Describe the morphology of the erythrocytes.
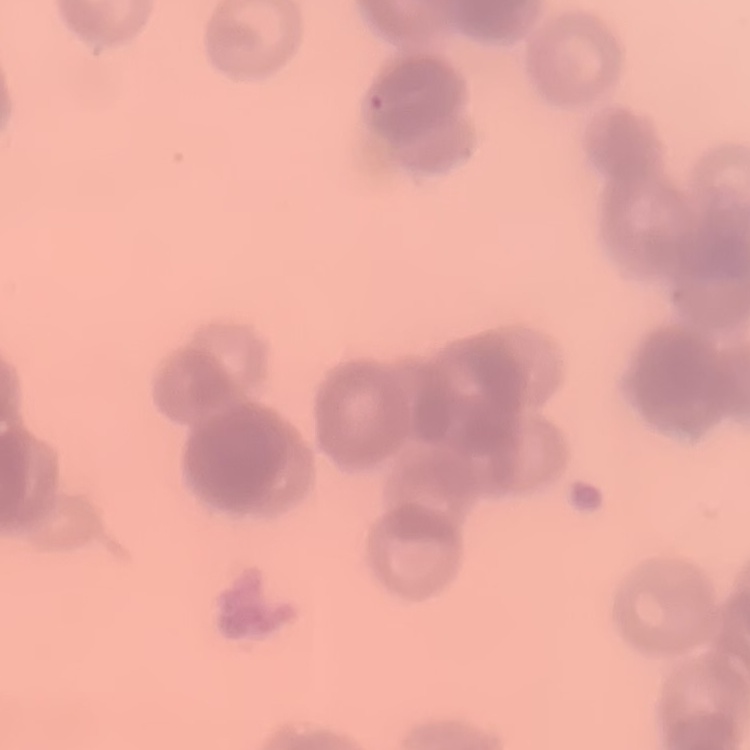
Rouleaux formation.

preparation = thin blood smear
image type = one tile cut from a larger photomicrograph
stain = Field's or Giemsa